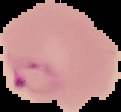

Summary:
  - Preparation: thin blood smear
  - Image type: cell region segmented out of the field of view; surrounding area masked to black
  - Image size: 121×112 pixels
  - Result: Plasmodium parasites identified